Point out each Plasmodium parasite.
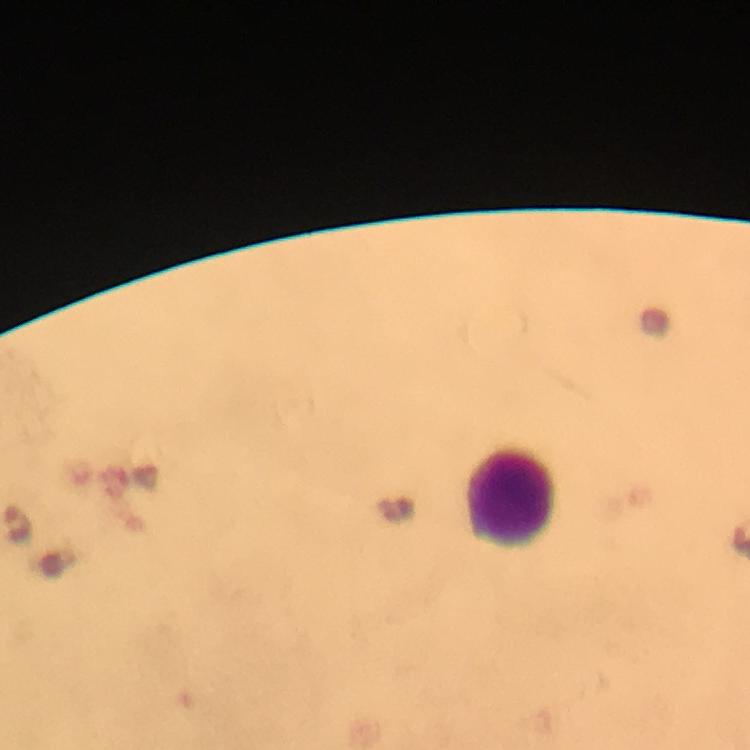

No Plasmodium parasites seen.

Approximate object centers, in pixels from the top-left corner.
Summary:
  - Leukocyte locations: (x=511, y=496)
  - Cropped from: one field of view
  - Immersion oil: applied
  - Capture: smartphone photograph through a microscope
  - Preparation: thick smear
  - Image size: 750×750 pixels
  - Context: from a diagnostic examination for malaria
  - Magnification: 100x
  - Stain: Giemsa